Assess this cell for malaria.
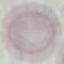

It is uninfected.

capture = smartphone camera at the microscope eyepiece
preparation = thin blood film
image type = automatically extracted cell patch, resized to 64 × 64 pixels
stain = Giemsa